Name the parasite shown.
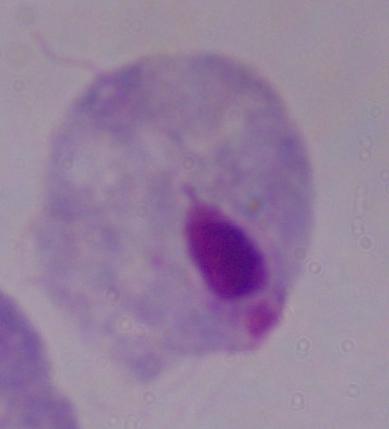
A trichomonad.

Photomicrograph. Captured at 1000x magnification.